Classify this cell by malaria status.
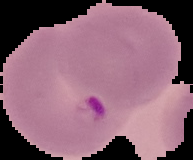
Parasitized.

preparation = thin blood smear
image size = 193×160 pixels
image type = segmented cell region on a black background